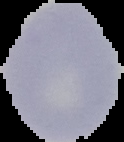

Cell region segmented out of the field of view; the surrounding area is masked to black. From a thin blood smear. Malaria status: uninfected. Image is 124×142 pixels.